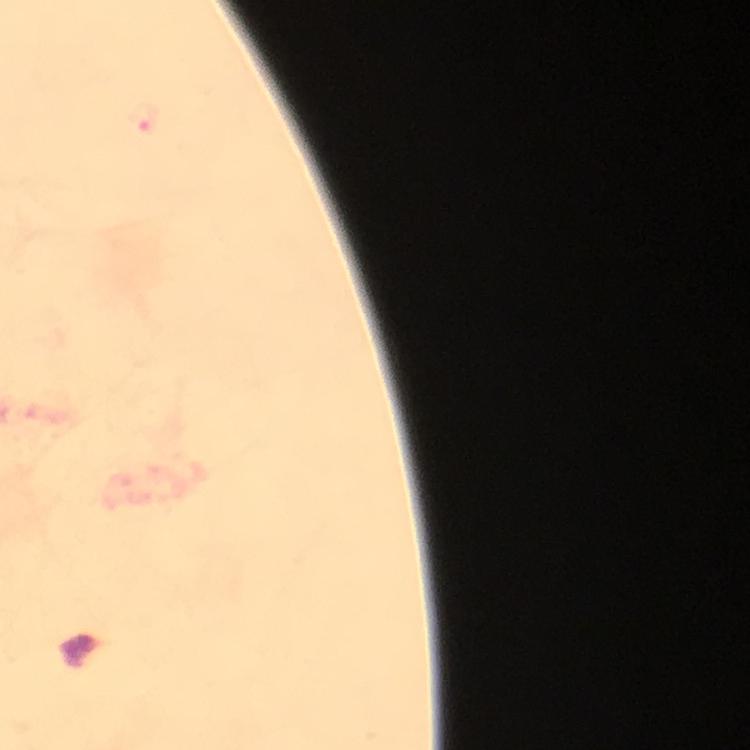

Approximate centers as {x, y} in pixels. Malaria parasite locations: {144, 117}. From a diagnostic examination for malaria. Immersion oil was used. Giemsa-stained preparation. Photographed through the microscope with a smartphone camera. Cropped region of a single field of view. 100x magnification. Thick smear. Image is 750×750 pixels.